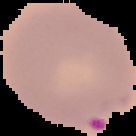

Summary:
  - Image type: segmented cell region with the area outside set to black
  - Image size: 136×136 pixels
  - Preparation: thin blood smear
  - Result: malaria parasites detected